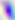

modality = photomicrograph
magnification = 400x
identification = Toxoplasma gondii